Classify this cell by malaria status.
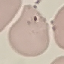

Uninfected.

stain = Giemsa
capture = smartphone through the microscope eyepiece
image type = cell patch, automatically extracted from a larger field of view and resized to 64 × 64 pixels
preparation = thin blood smear